Report the malaria status of this cell.
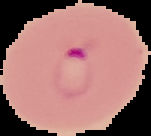
It is parasitized.

Image is 151×136 pixels. From a thin blood film. Segmented cell region on a black background.